Assess this cell for malaria.
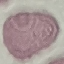

Uninfected.

preparation: thin smear
image_type: automatically extracted cell patch, resized to 64 × 64 pixels
capture: smartphone camera at the microscope eyepiece
stain: Giemsa